Evaluate for parasitized red blood cells.
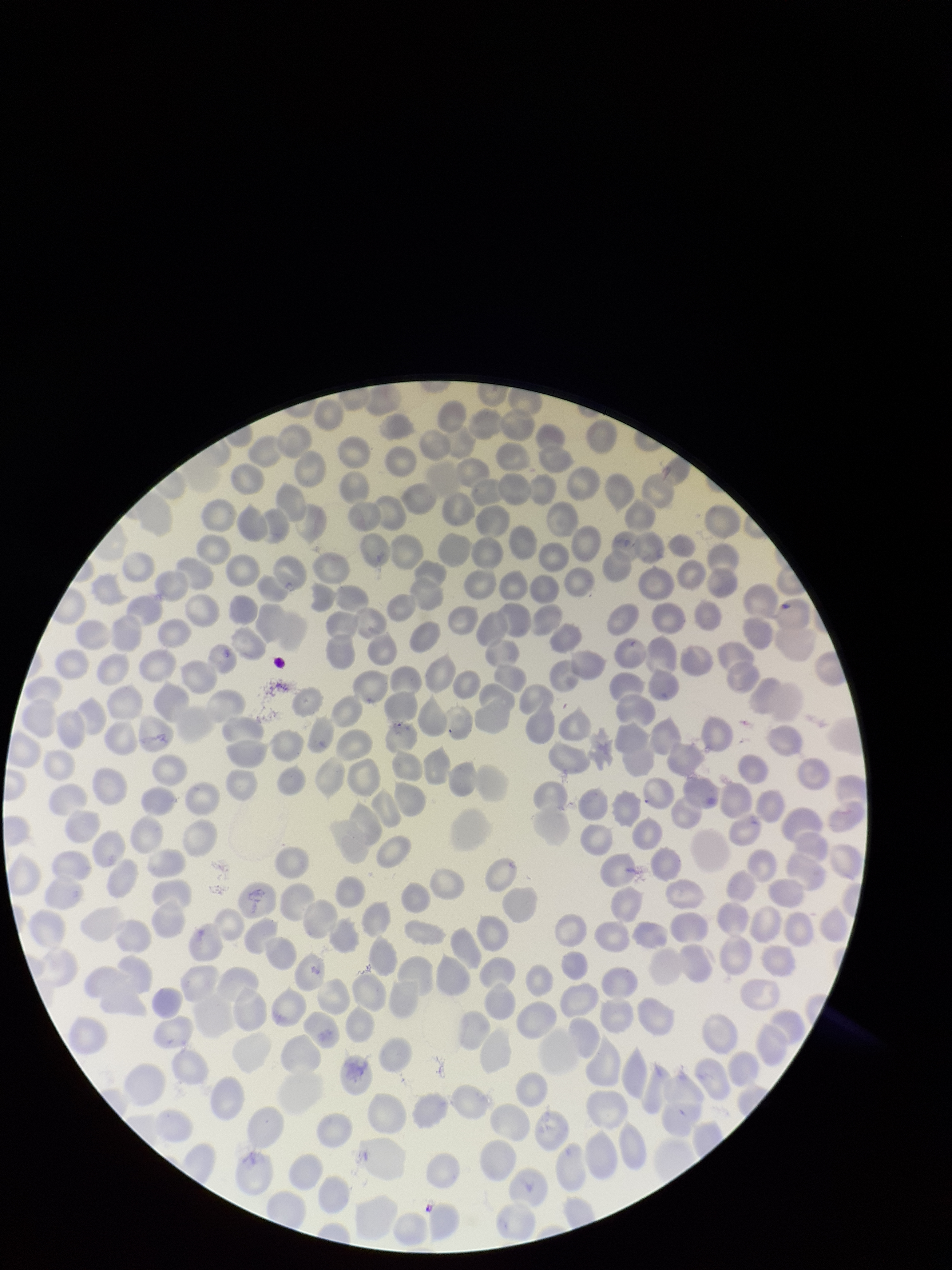
None seen.

Species reported for this patient: Plasmodium falciparum. Parasitized red blood cell count: 0. Red blood cell count: 247. Preparation: thin smear. Photographed through the microscope eyepiece with a smartphone camera. Patient malaria status: positive. Single field of view. Stained with Giemsa. Image is 952×1270 pixels.